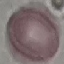

result = no malaria parasites seen
image type = automatically extracted cell patch, resized to 64 × 64 pixels
stain = Giemsa
preparation = thin blood film
capture = smartphone camera at the microscope eyepiece